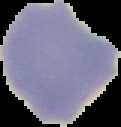

image type = cell region segmented out of the field of view; surrounding area masked to black
image size = 121×127 pixels
preparation = thin blood smear
malaria status = uninfected